Classify this cell by malaria status.
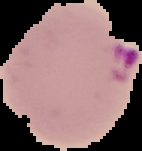
It is parasitized.

Image is 142×151 pixels. From a thin blood film. Segmented cell region on a black background.